Locate every uninfected red blood cell.
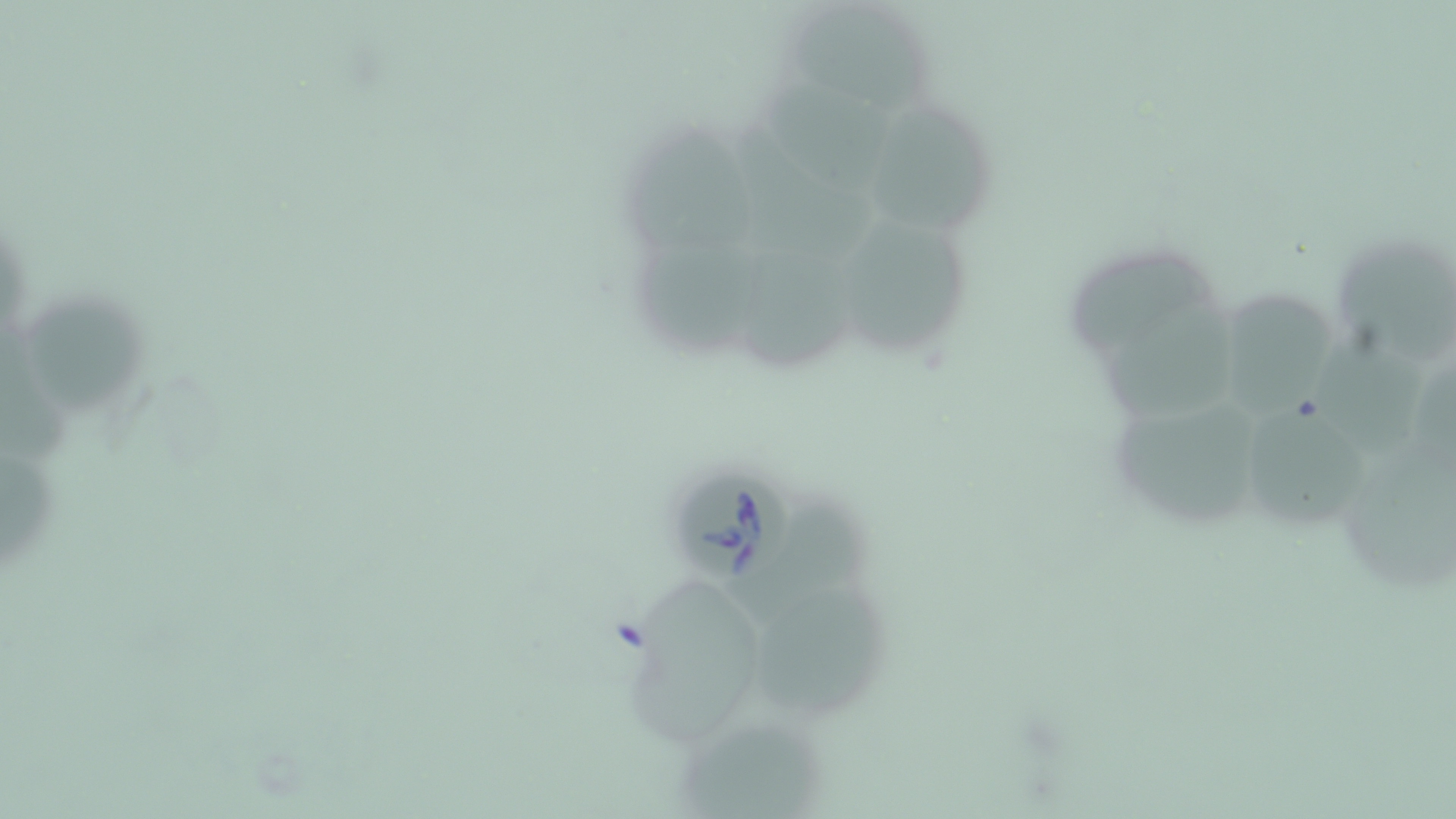
Approximate bounding boxes as (x1, y1, x2, y2) in pixels.
Uninfected red blood cells: (789, 1, 926, 113), (759, 78, 896, 189), (864, 96, 995, 234), (733, 120, 874, 257), (625, 123, 759, 249), (841, 212, 972, 356), (634, 233, 764, 349), (740, 239, 870, 373), (1336, 239, 1456, 369), (1072, 248, 1222, 354), (1225, 281, 1332, 422), (22, 287, 151, 420), (1100, 298, 1248, 424), (1, 336, 77, 472), (1318, 339, 1429, 474), (1107, 391, 1272, 533), (1254, 408, 1368, 521), (1343, 445, 1456, 592), (0, 449, 59, 576), (738, 498, 879, 618), (635, 576, 755, 741), (753, 593, 893, 722), (673, 709, 831, 819).

Babesia divergens-infected red blood cell locations: (675, 467, 794, 588). Slide-level diagnosis: Babesia divergens. Optical microscopy. May-Grünwald-Giemsa-stained preparation. Image is 1456×819 pixels. Single field of view. Captured at 1000x magnification. Thin blood film.